Evaluate for Plasmodium parasites.
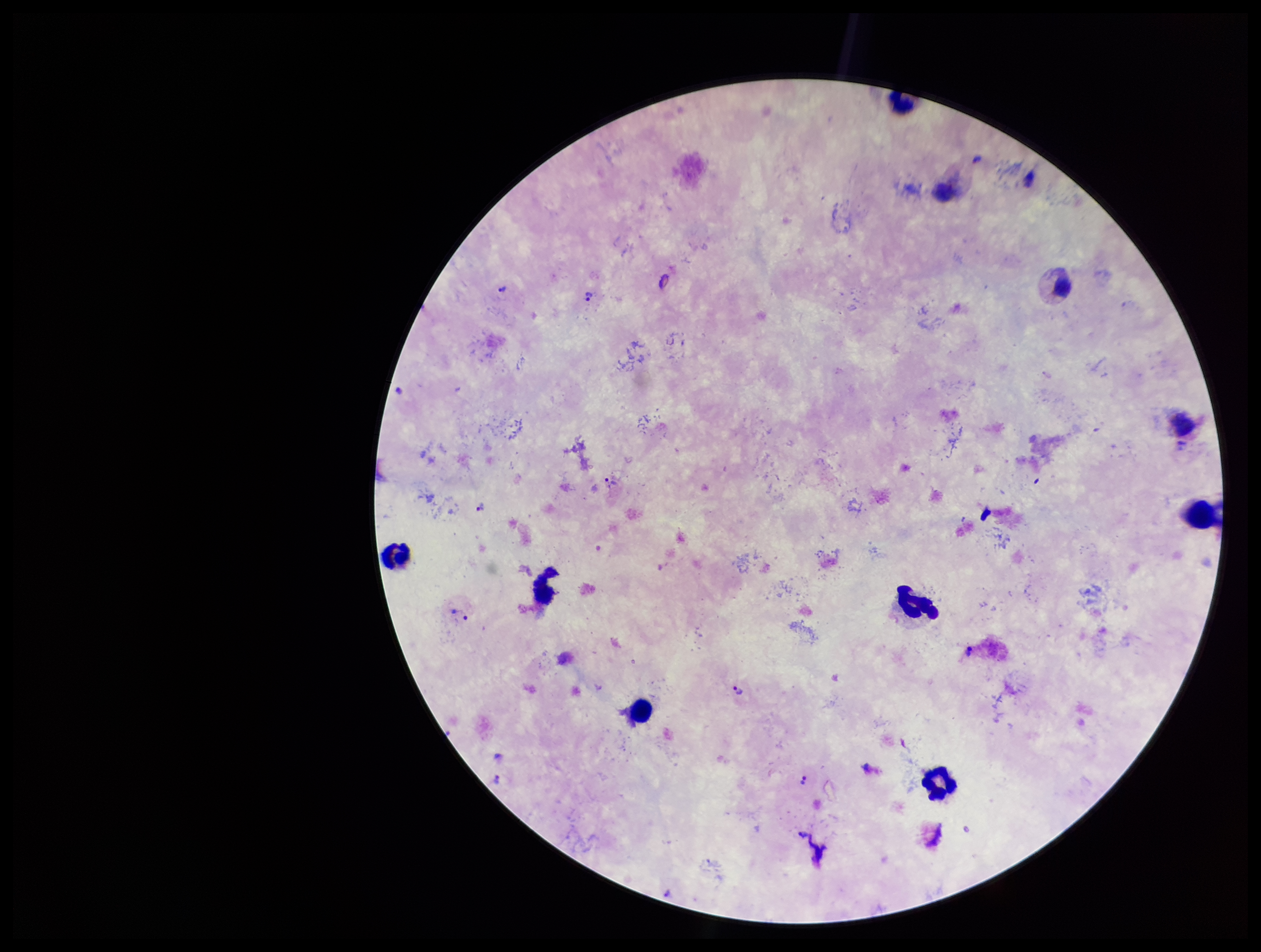

Detected.

Summary:
  - Parasite count: 8
  - Patient malaria status: infected
  - Preparation: thick blood smear
  - Field of view: one from this slide
  - Capture: smartphone photograph through the microscope eyepiece
  - Leukocyte count: 8
  - Image size: 1261×952 pixels
  - Stain: Giemsa
  - Species reported for this patient: Plasmodium vivax